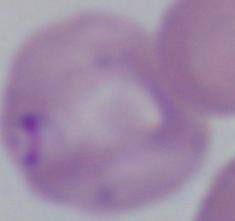

identification = Babesia
magnification = 1000x
modality = micrograph